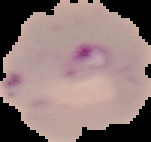
malaria_status: parasitized
preparation: thin blood smear
image_type: cell region segmented out of the field of view; surrounding area masked to black
image_size: 151×142 pixels